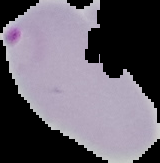
image size = 160×163 pixels
result = Plasmodium parasites detected
image type = segmented cell region on a black background
preparation = thin blood film